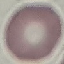

Summary:
  - Malaria status: uninfected
  - Image type: cell patch, automatically extracted from a larger field of view and resized to 64 × 64 pixels
  - Stain: Giemsa
  - Capture: smartphone through the microscope eyepiece
  - Preparation: thin blood smear